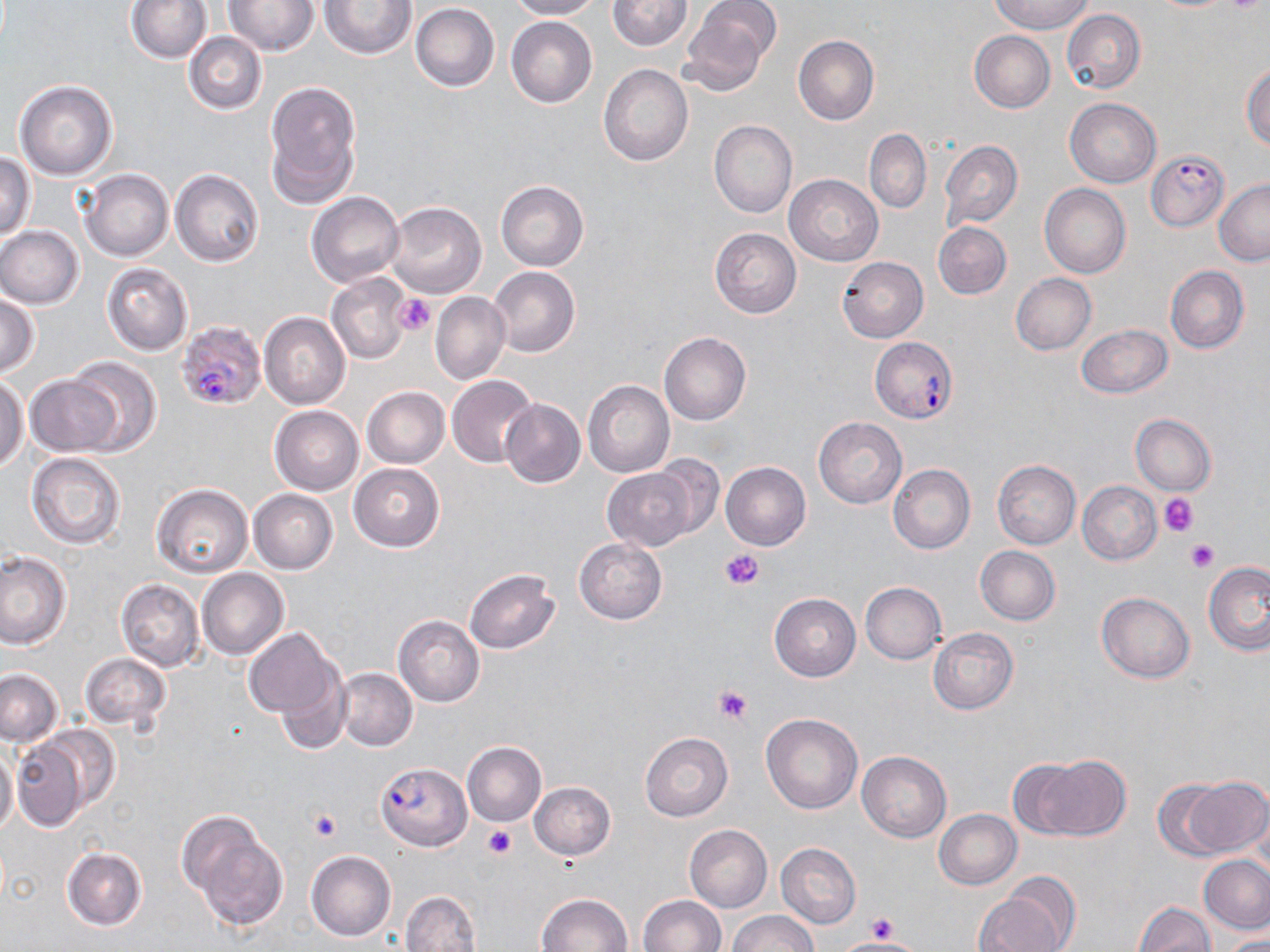
slide-level diagnosis = Plasmodium falciparum
magnification = 1000x
Plasmodium falciparum-infected red blood cell locations = approximate bounding boxes as (x1, y1, x2, y2) in pixels: (1147, 148, 1227, 230), (177, 320, 266, 412), (871, 337, 957, 423), (378, 762, 469, 850)
stain = May-Grünwald-Giemsa
image size = 1270×952 pixels
uninfected red blood cell locations = approximate bounding boxes as (x1, y1, x2, y2) in pixels: (126, 0, 211, 63), (505, 0, 600, 20), (607, 0, 692, 51), (680, 0, 780, 94), (991, 0, 1094, 35), (223, 1, 320, 55), (321, 1, 417, 59), (320, 2, 498, 71), (411, 3, 499, 91), (1062, 9, 1146, 94), (506, 16, 598, 108), (968, 31, 1055, 113), (184, 32, 266, 115), (793, 35, 879, 125), (1241, 62, 1270, 150), (598, 65, 693, 166), (14, 79, 118, 182), (264, 82, 360, 205), (1064, 98, 1161, 187), (709, 120, 797, 218), (864, 129, 931, 213), (939, 140, 1022, 229), (0, 154, 35, 239), (81, 169, 173, 262), (170, 169, 264, 266), (784, 174, 883, 265), (495, 179, 589, 272), (1213, 179, 1270, 265), (1039, 183, 1131, 279), (307, 191, 403, 286), (385, 202, 487, 299), (933, 221, 1012, 299), (0, 226, 83, 309), (709, 228, 802, 318), (838, 257, 928, 342), (101, 262, 193, 355), (487, 266, 581, 358), (1165, 266, 1250, 354), (326, 273, 412, 365), (1010, 273, 1097, 355), (431, 291, 509, 386), (0, 292, 39, 377), (259, 312, 351, 409), (1077, 324, 1173, 399), (658, 332, 751, 425), (66, 358, 161, 455), (24, 374, 122, 457), (447, 375, 539, 469), (0, 376, 27, 470), (583, 380, 674, 478), (361, 386, 449, 468), (499, 397, 585, 487), (269, 404, 364, 495), (258, 412, 347, 573), (1131, 414, 1216, 496), (813, 417, 907, 509), (26, 453, 125, 549), (642, 456, 724, 545), (992, 460, 1081, 549), (721, 461, 811, 550), (349, 463, 444, 551), (887, 464, 976, 554), (602, 466, 701, 550), (1077, 481, 1162, 565), (151, 484, 252, 578), (249, 489, 337, 573), (574, 538, 668, 624), (974, 546, 1060, 626), (0, 551, 70, 649), (1203, 561, 1270, 655), (197, 568, 289, 660), (465, 568, 559, 654), (117, 579, 204, 671), (859, 582, 946, 665), (1096, 592, 1195, 684), (769, 593, 860, 681), (393, 615, 484, 707), (242, 628, 339, 724), (928, 628, 1019, 714), (80, 653, 171, 733), (0, 668, 64, 747), (272, 668, 350, 757), (334, 669, 418, 751), (761, 713, 863, 813), (35, 725, 120, 819), (639, 732, 732, 821), (9, 734, 93, 832), (5, 741, 35, 832), (462, 742, 546, 826), (0, 745, 18, 837), (856, 750, 952, 842), (1029, 754, 1131, 842), (1007, 758, 1087, 840), (1171, 776, 1268, 859), (530, 782, 616, 860), (933, 809, 1022, 890), (179, 812, 287, 933), (683, 825, 772, 913), (775, 842, 862, 928), (61, 847, 148, 930), (306, 850, 397, 941), (1199, 854, 1270, 933), (975, 882, 1072, 952), (400, 891, 482, 952), (537, 892, 632, 952), (637, 895, 725, 952), (1134, 902, 1216, 952), (727, 911, 819, 952), (1220, 932, 1270, 951)
modality = optical microscopy
preparation = thin blood smear
platelet locations = approximate bounding boxes as (x1, y1, x2, y2) in pixels: (394, 293, 438, 336), (1159, 493, 1197, 536), (1187, 540, 1219, 571), (720, 547, 764, 590), (714, 685, 752, 725), (308, 809, 341, 842), (483, 824, 516, 859), (867, 912, 899, 940)
field of view = single